Report the malaria status of this cell.
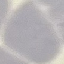
Uninfected.

Thin smear of blood. Acquired by smartphone through the microscope eyepiece. Automatically extracted cell patch, resized to 64 × 64 pixels. Giemsa-stained preparation.